Classify this cell by malaria status.
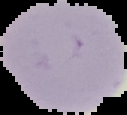

It is uninfected.

Summary:
  - Preparation: thin blood smear
  - Image type: cell region segmented out of the field of view; surrounding area masked to black
  - Image size: 127×115 pixels